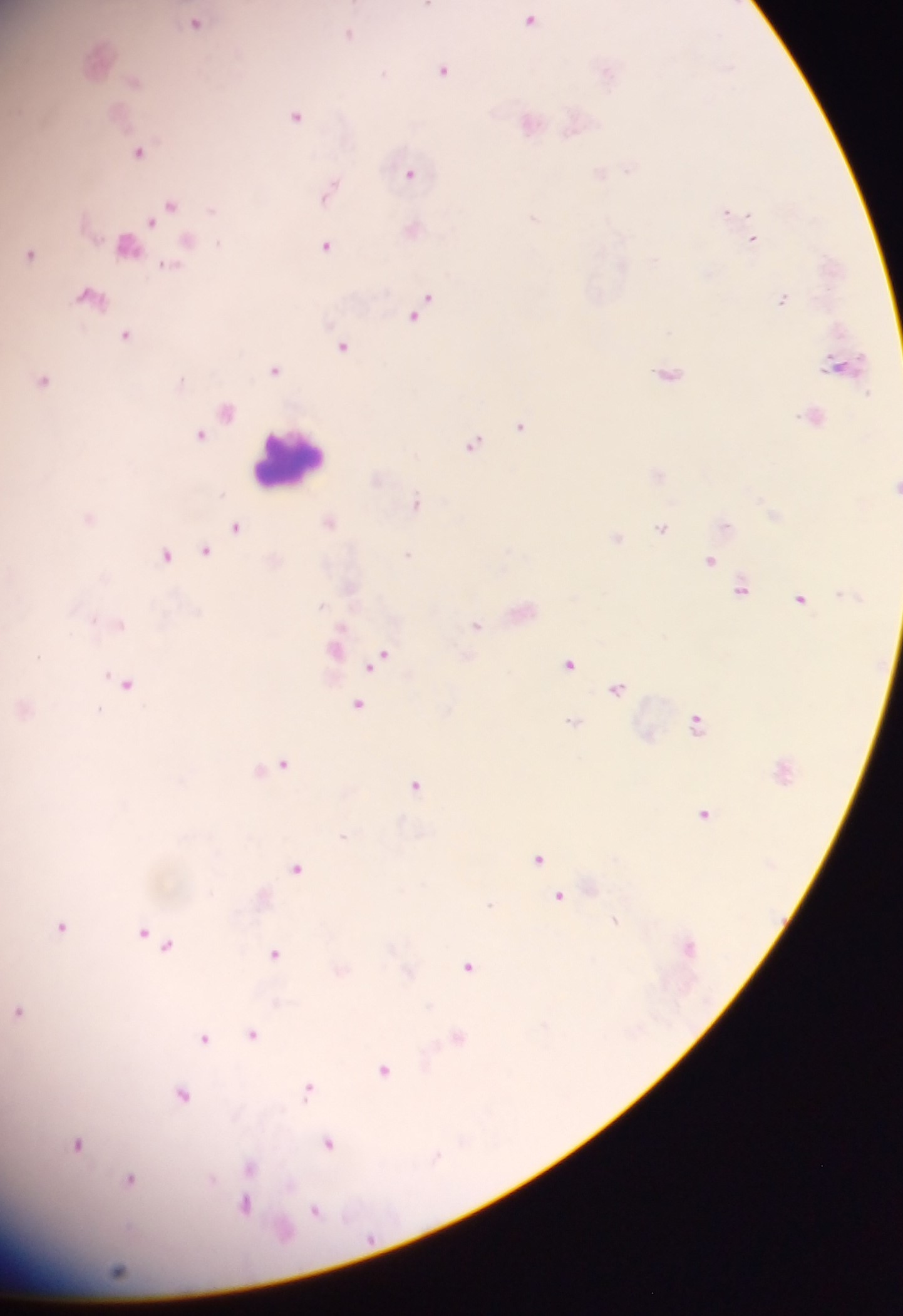

Approximate centers as x y in pixels.
Summary:
  - Malaria parasite locations: 428 5; 529 20; 195 22; 348 35; 443 69; 383 73; 295 115; 137 152; 408 173; 327 192; 169 206; 726 212; 752 239; 127 245; 326 245; 30 254; 166 265; 91 297; 781 299; 422 308; 125 335; 343 346; 274 369; 667 373; 42 380; 226 411; 520 425; 200 434; 472 444; 416 503; 89 519; 329 522; 235 527; 660 528; 616 539; 204 551; 408 554; 165 555; 710 561; 740 588; 799 599; 120 624; 475 625; 38 656; 379 659; 568 663; 126 683; 617 689; 357 705; 98 710; 572 722; 696 723; 280 764; 416 785; 704 814; 343 836; 538 858; 297 868; 558 896; 489 904; 614 921; 62 926; 144 935; 155 941; 273 953; 468 967; 19 1011; 253 1034; 458 1038; 203 1039; 384 1071; 308 1090; 182 1094; 328 1143; 78 1145; 248 1169; 129 1181; 243 1205; 314 1210
  - Leukocyte locations: 288 460
  - Capture: mobile-phone photograph through a microscope
  - Image size: 903×1316 pixels
  - Country: Ghana
  - Preparation: thick blood film
  - Field of view: single